Assess for malaria.
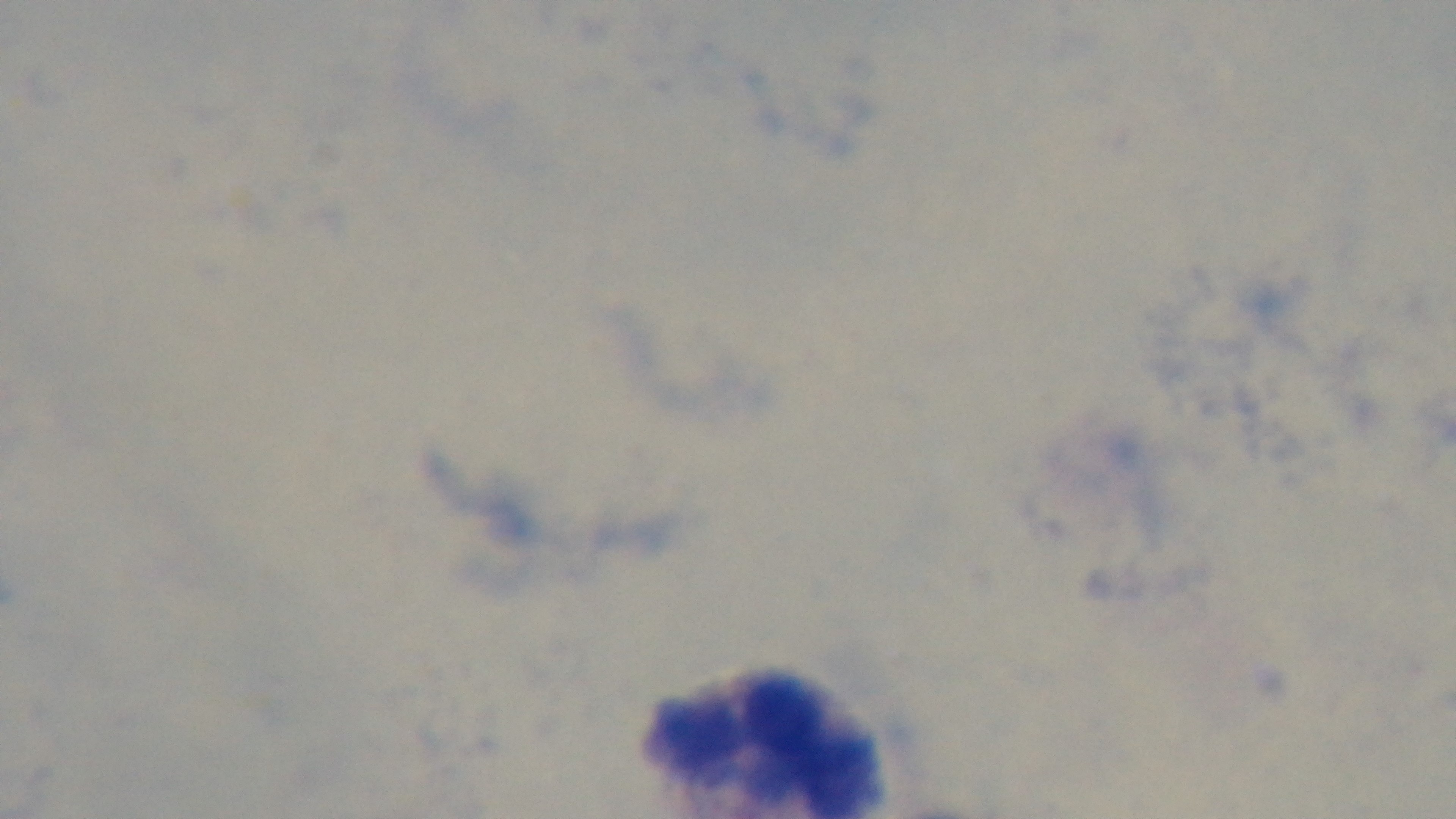

It is uninfected.

Summary:
  - Objective: 100x oil immersion
  - Modality: light microscopy
  - Preparation: thick smear
  - Capture: mounted 4K digital camera
  - Stain: Giemsa
  - Field of view: one from the slide